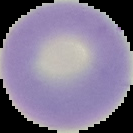

image type = segmented cell region on a black background
malaria status = uninfected
image size = 133×133 pixels
preparation = thin blood smear